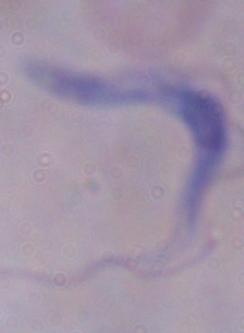 Captured at 1000x magnification. A trypanosome is shown. Photomicrograph.